Point out each Plasmodium parasite.
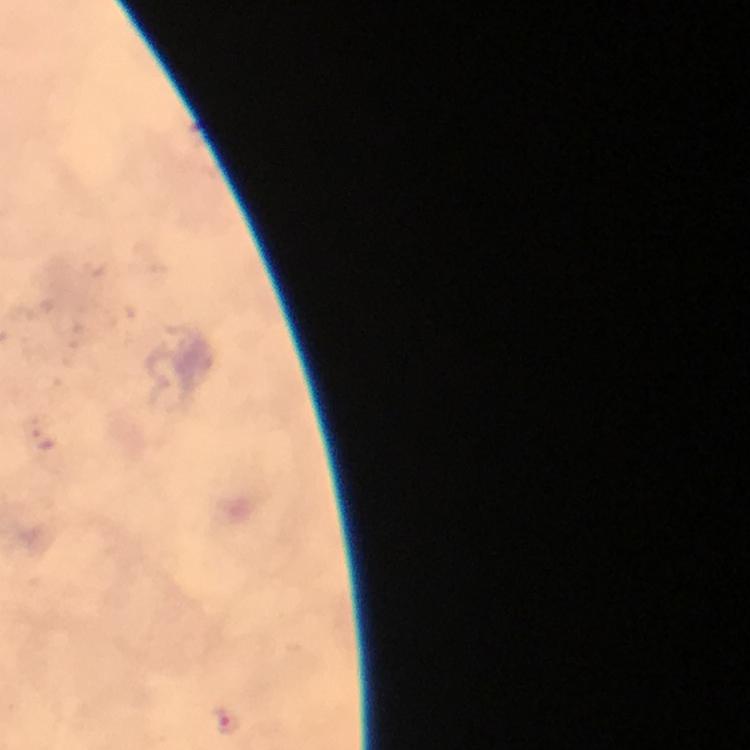

Approximate centers as (x, y) in pixels.
Plasmodium parasites: (225, 720).

Summary:
  - Immersion oil: used
  - Capture: smartphone photograph through a microscope
  - Preparation: thick smear
  - Stain: Giemsa
  - Magnification: 100x
  - Cropped from: a single field of view
  - Image size: 750×750 pixels
  - Context: from a malaria diagnostic workup